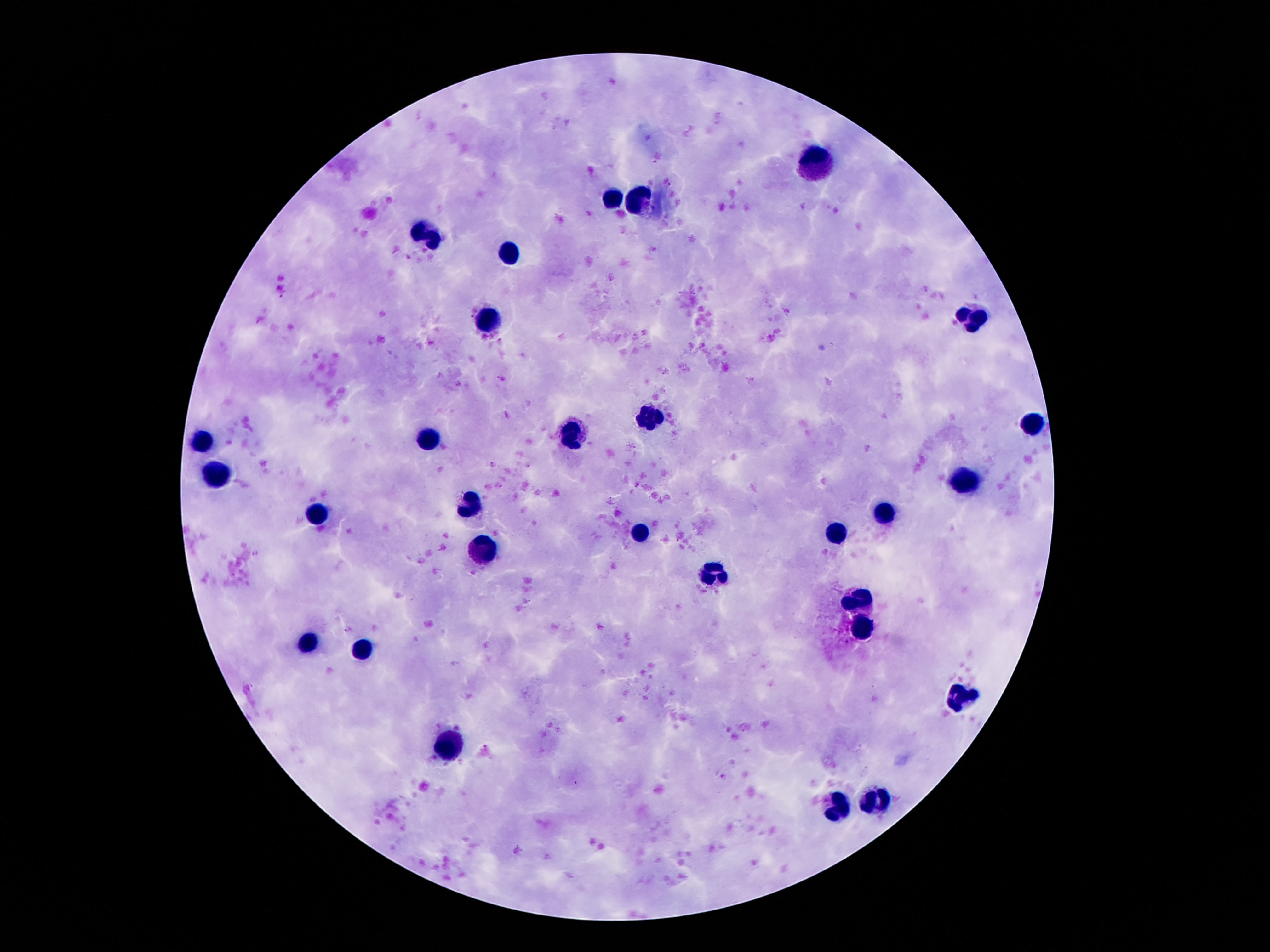 Approximate object centers, in pixels from the top-left corner. Leukocyte locations: (x=816, y=164), (x=614, y=197), (x=637, y=200), (x=427, y=231), (x=511, y=248), (x=486, y=318), (x=971, y=319), (x=652, y=417), (x=1034, y=424), (x=572, y=431), (x=427, y=435), (x=203, y=444), (x=218, y=477), (x=961, y=481), (x=469, y=504), (x=885, y=513), (x=318, y=517), (x=639, y=531), (x=833, y=532), (x=480, y=550), (x=713, y=572), (x=862, y=599), (x=862, y=629), (x=310, y=641), (x=362, y=648), (x=961, y=698), (x=449, y=746), (x=877, y=799), (x=837, y=807). Patient malaria status: not infected. 100x magnification. Image is 1270×952 pixels. Single field of view. Thick peripheral-blood smear. Giemsa-stained preparation. Photographed through the microscope eyepiece with a smartphone camera.